Locate every blood parasite and identify its species.
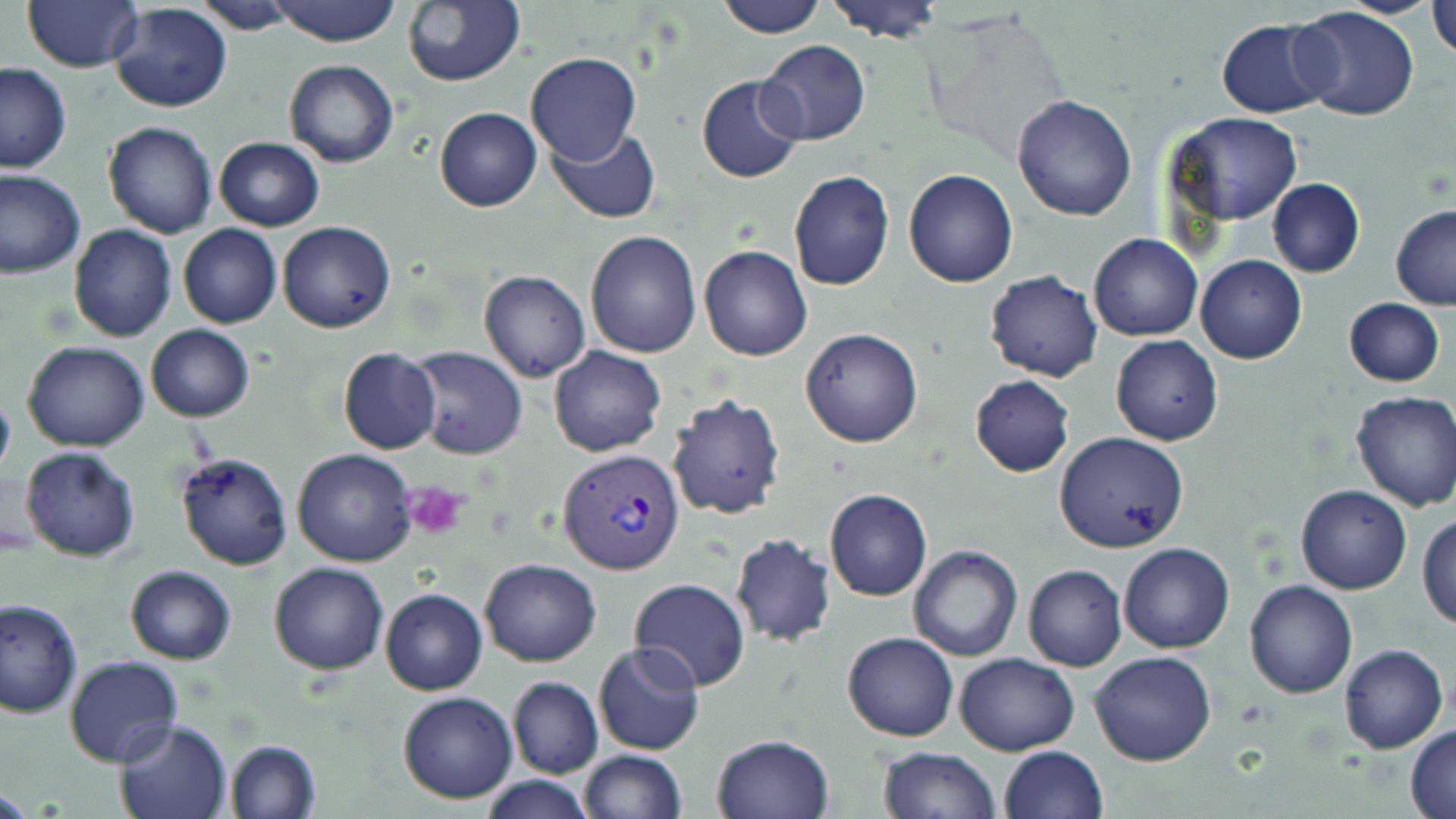

Approximate bounding boxes as (x1,y1)-(x2,y2) corner pairs in pixels.
Plasmodium vivax-infected red blood cells: (558,447)-(686,575).
No Plasmodium falciparum, Plasmodium ovale, Plasmodium malariae, Babesia divergens, or Trypanosoma brucei observed.

slide-level diagnosis = Plasmodium vivax
image size = 1456×819 pixels
platelet locations = approximate bounding boxes as (x1,y1)-(x2,y2) corner pairs in pixels: (403,482)-(469,539)
magnification = 1000x
preparation = thin blood film
field of view = one of a larger specimen
stain = May-Grünwald-Giemsa
modality = optical microscopy
uninfected red blood cell locations = approximate bounding boxes as (x1,y1)-(x2,y2) corner pairs in pixels: (270,0)-(402,46), (402,0)-(526,86), (715,0)-(826,38), (823,0)-(946,43), (22,1)-(143,74), (194,1)-(304,32), (108,2)-(233,114), (1428,2)-(1455,59), (1292,7)-(1420,123), (1216,19)-(1333,118), (755,39)-(870,147), (526,53)-(641,166), (283,60)-(398,167), (0,61)-(72,173), (696,75)-(805,183), (1012,94)-(1136,221), (434,107)-(541,212), (1165,111)-(1303,226), (103,122)-(217,239), (548,126)-(659,223), (213,138)-(324,231), (903,168)-(1017,287), (0,169)-(86,278), (788,171)-(895,291), (1267,177)-(1364,277), (1390,205)-(1456,311), (277,221)-(396,334), (68,224)-(178,343), (177,225)-(282,329), (585,230)-(702,358), (1088,233)-(1202,341), (699,245)-(813,362), (1196,254)-(1306,364), (985,269)-(1104,383), (478,270)-(591,383), (1344,298)-(1444,387), (145,325)-(254,421), (800,328)-(924,448), (1110,334)-(1222,446), (23,341)-(151,452), (548,346)-(665,457), (337,347)-(441,455), (404,347)-(527,460), (971,375)-(1075,476), (0,383)-(15,486), (1350,391)-(1456,513), (665,392)-(785,521), (1053,431)-(1189,554), (20,445)-(140,562), (292,448)-(419,566), (175,452)-(292,571), (1296,485)-(1412,594), (824,488)-(932,602), (1418,511)-(1455,630), (729,533)-(837,647), (1117,541)-(1234,653), (907,545)-(1024,662), (479,559)-(602,666), (268,562)-(389,675), (1022,564)-(1128,671), (124,566)-(236,664), (627,579)-(750,691), (1244,579)-(1357,698), (380,588)-(487,695), (0,598)-(81,718), (843,632)-(959,741), (593,642)-(704,756), (1339,642)-(1448,754), (1088,650)-(1217,766), (954,651)-(1080,756), (63,655)-(182,768), (508,677)-(603,778), (397,691)-(519,804), (115,717)-(234,819), (1406,724)-(1456,819), (711,733)-(836,819), (224,738)-(321,819), (999,745)-(1107,819), (876,746)-(999,819), (577,749)-(687,819), (480,775)-(593,819)